Identify the blood parasite species.
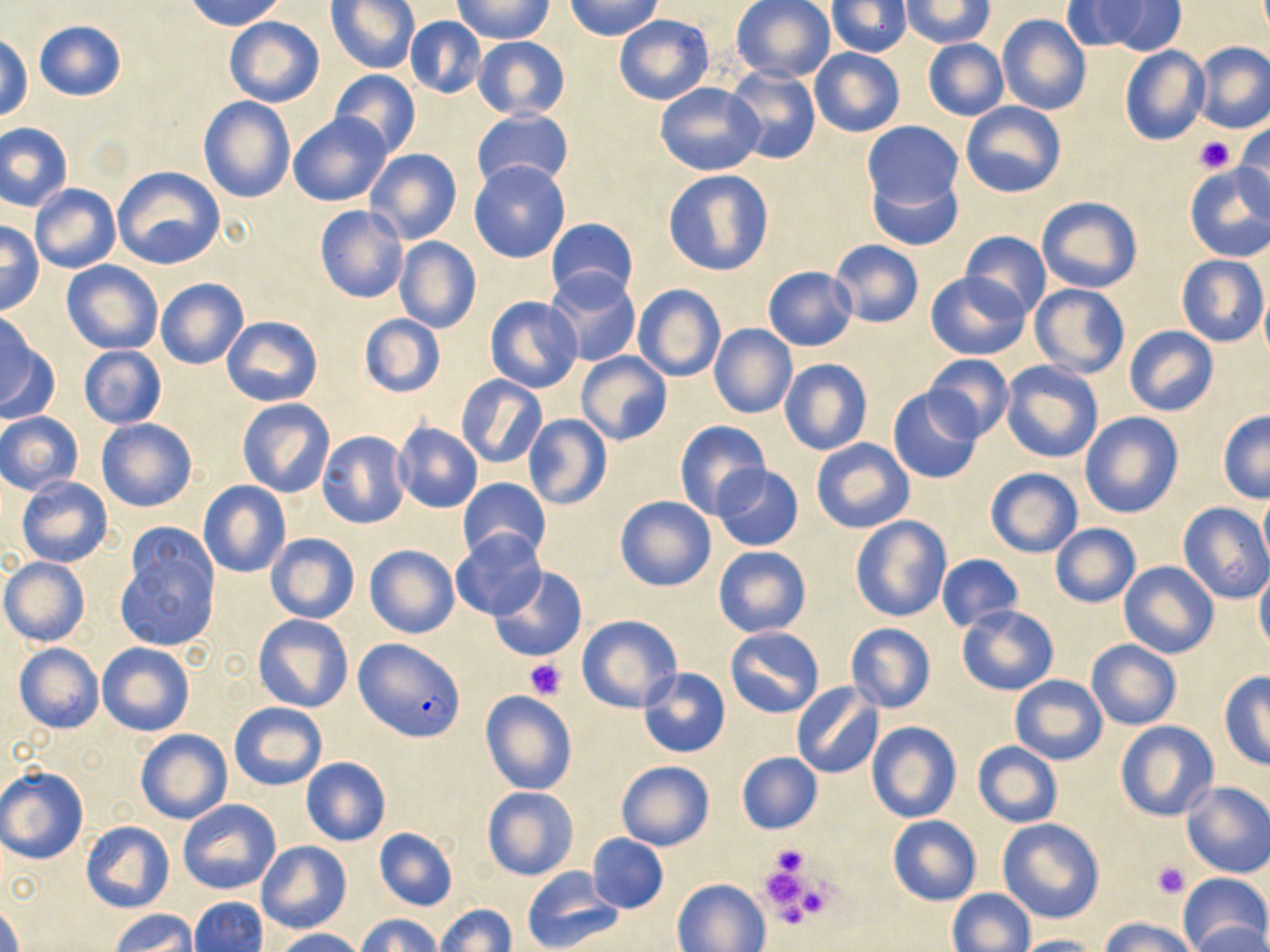
Plasmodium falciparum.

Summary:
  - Coordinate format: approximate bounding boxes as (x1,y1)-(x2,y2) corner pairs in pixels
  - Uninfected red blood cell locations: (183,0)-(287,32), (327,0)-(419,73), (565,0)-(661,41), (731,0)-(836,84), (826,0)-(911,57), (900,1)-(994,49), (1060,1)-(1149,53), (1101,1)-(1186,56), (452,2)-(551,42), (613,14)-(714,106), (996,14)-(1091,117), (404,17)-(487,99), (224,18)-(324,106), (33,20)-(126,101), (0,34)-(32,123), (472,35)-(570,120), (922,38)-(1009,121), (1191,41)-(1270,133), (1119,46)-(1209,146), (809,47)-(904,137), (722,65)-(820,165), (330,69)-(421,158), (655,81)-(763,176), (198,96)-(295,203), (960,101)-(1065,198), (470,108)-(573,193), (288,112)-(394,208), (861,121)-(963,214), (1,122)-(73,212), (1233,125)-(1270,211), (363,148)-(461,245), (468,160)-(570,262), (1183,162)-(1270,260), (113,166)-(225,269), (663,169)-(775,275), (867,171)-(964,252), (30,183)-(121,273), (1036,196)-(1142,292), (314,205)-(408,303), (546,216)-(637,302), (0,223)-(43,313), (959,230)-(1050,319), (392,237)-(482,334), (828,239)-(924,328), (1177,254)-(1267,346), (62,260)-(164,354), (762,266)-(858,351), (546,269)-(642,368), (925,271)-(1030,358), (155,276)-(249,370), (1030,283)-(1130,377), (632,284)-(725,382), (1260,288)-(1270,368), (484,296)-(583,393), (357,313)-(446,397), (0,315)-(53,422), (222,316)-(322,406), (708,323)-(797,419), (1124,326)-(1217,416), (79,345)-(167,428), (575,351)-(671,446), (923,355)-(1012,440), (779,359)-(873,456), (1000,359)-(1103,464), (455,375)-(547,469), (887,387)-(985,484), (237,398)-(336,498), (1217,410)-(1270,503), (1,411)-(85,495), (1080,411)-(1183,519), (522,415)-(610,509), (96,418)-(198,512), (673,420)-(770,520), (392,422)-(483,513), (317,431)-(411,529), (811,438)-(915,534), (712,465)-(804,552), (985,467)-(1083,557), (15,476)-(113,567), (456,477)-(550,563), (199,480)-(290,577), (1259,487)-(1270,573), (614,494)-(717,593), (1178,502)-(1270,604), (849,516)-(950,622), (116,524)-(220,653), (1048,524)-(1142,609), (449,530)-(547,622), (265,532)-(360,624), (365,545)-(459,638), (713,545)-(812,638), (935,553)-(1023,632), (1,558)-(89,646), (1118,561)-(1218,658), (489,566)-(587,662), (1254,569)-(1270,657), (956,604)-(1058,694), (252,614)-(353,712), (576,614)-(683,713), (844,623)-(935,714), (725,626)-(824,718), (1085,640)-(1182,731), (98,642)-(195,736), (14,643)-(103,733), (638,668)-(730,758), (1219,672)-(1270,770), (1010,674)-(1108,764), (791,682)-(884,779), (479,690)-(577,795), (230,702)-(328,791), (866,721)-(960,822), (1116,721)-(1219,821), (136,728)-(233,823), (972,741)-(1062,828), (736,752)-(822,834), (300,756)-(391,846), (616,760)-(714,851), (0,766)-(88,864), (1181,781)-(1270,878), (481,787)-(580,880), (178,799)-(281,894), (888,815)-(981,906), (997,818)-(1104,924), (80,820)-(176,915), (374,828)-(458,911), (587,833)-(668,914), (257,842)-(350,933), (520,867)-(624,952), (1178,871)-(1270,952), (674,878)-(770,951), (946,889)-(1035,952), (188,897)-(267,952), (0,901)-(22,952), (435,903)-(516,952), (112,911)-(196,952), (356,913)-(443,951), (1101,917)-(1196,952), (1192,922)-(1270,952), (273,928)-(366,952), (1010,934)-(1102,952)
  - Platelet locations: (1195,136)-(1235,174), (524,659)-(564,700), (768,843)-(813,884), (1150,861)-(1191,897), (760,864)-(823,929)
  - Plasmodium falciparum-infected red blood cell locations: (353,638)-(465,741)
  - Magnification: 1000x
  - Field of view: single
  - Stain: May-Grünwald-Giemsa
  - Image size: 1270×952 pixels
  - Modality: optical microscopy
  - Preparation: thin blood smear